State which parasite is depicted.
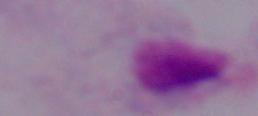
This is a trichomonad.

{
  "magnification": "1000x",
  "modality": "photomicrograph"
}